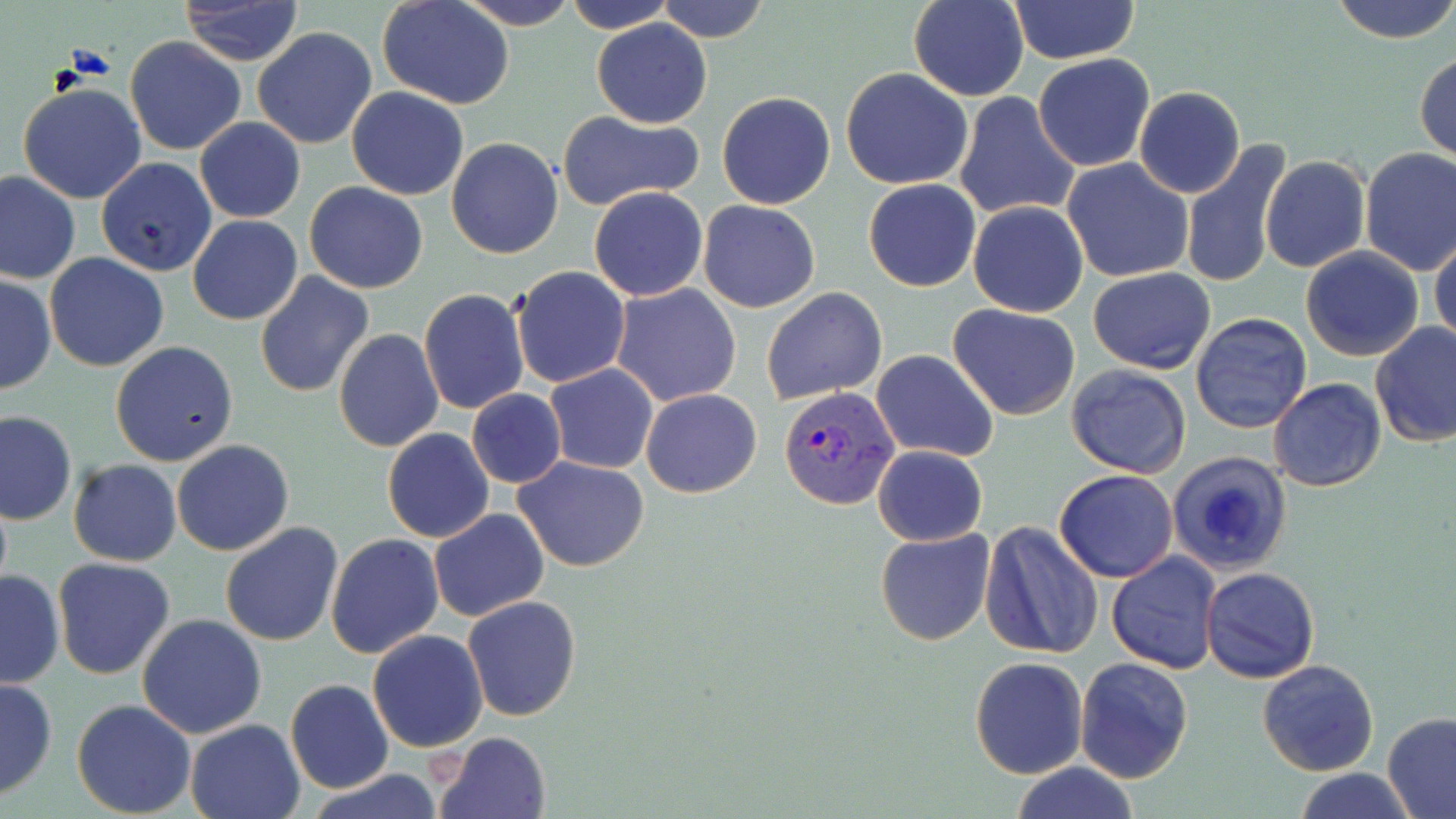

Summary:
  - Coordinate format: approximate bounding boxes as named x1/y1/x2/y2 corners in pixels
  - Uninfected red blood cell locations: (x1=455, y1=0, x2=581, y2=30), (x1=563, y1=0, x2=678, y2=32), (x1=654, y1=0, x2=769, y2=43), (x1=908, y1=0, x2=1030, y2=101), (x1=1008, y1=0, x2=1140, y2=63), (x1=1328, y1=0, x2=1456, y2=45), (x1=378, y1=1, x2=514, y2=109), (x1=179, y1=2, x2=305, y2=65), (x1=591, y1=18, x2=712, y2=128), (x1=252, y1=27, x2=379, y2=149), (x1=125, y1=37, x2=247, y2=157), (x1=1415, y1=50, x2=1456, y2=163), (x1=1033, y1=53, x2=1156, y2=172), (x1=840, y1=68, x2=974, y2=190), (x1=17, y1=81, x2=148, y2=204), (x1=720, y1=81, x2=971, y2=198), (x1=347, y1=86, x2=469, y2=200), (x1=1134, y1=86, x2=1244, y2=199), (x1=716, y1=92, x2=836, y2=209), (x1=955, y1=93, x2=1079, y2=219), (x1=1159, y1=109, x2=1275, y2=248), (x1=557, y1=110, x2=703, y2=213), (x1=194, y1=118, x2=306, y2=222), (x1=446, y1=138, x2=563, y2=258), (x1=1180, y1=142, x2=1292, y2=289), (x1=1358, y1=148, x2=1456, y2=276), (x1=1260, y1=156, x2=1370, y2=273), (x1=96, y1=157, x2=217, y2=276), (x1=1062, y1=157, x2=1195, y2=283), (x1=1, y1=171, x2=81, y2=286), (x1=862, y1=177, x2=981, y2=292), (x1=304, y1=182, x2=430, y2=293), (x1=589, y1=186, x2=709, y2=300), (x1=697, y1=200, x2=820, y2=314), (x1=967, y1=201, x2=1089, y2=317), (x1=188, y1=215, x2=303, y2=325), (x1=1430, y1=232, x2=1455, y2=353), (x1=211, y1=241, x2=355, y2=378), (x1=1300, y1=248, x2=1424, y2=361), (x1=43, y1=254, x2=169, y2=372), (x1=512, y1=265, x2=630, y2=388), (x1=1088, y1=267, x2=1216, y2=375), (x1=254, y1=273, x2=374, y2=397), (x1=0, y1=274, x2=57, y2=395), (x1=611, y1=283, x2=743, y2=407), (x1=761, y1=287, x2=888, y2=404), (x1=418, y1=288, x2=529, y2=415), (x1=948, y1=303, x2=1081, y2=420), (x1=1189, y1=313, x2=1312, y2=433), (x1=1369, y1=322, x2=1456, y2=447), (x1=334, y1=328, x2=444, y2=450), (x1=110, y1=341, x2=239, y2=466), (x1=871, y1=349, x2=999, y2=461), (x1=1065, y1=364, x2=1193, y2=478), (x1=544, y1=365, x2=659, y2=474), (x1=1269, y1=377, x2=1386, y2=492), (x1=641, y1=387, x2=763, y2=497), (x1=466, y1=390, x2=566, y2=487), (x1=0, y1=409, x2=77, y2=524), (x1=383, y1=429, x2=494, y2=543), (x1=171, y1=439, x2=295, y2=556), (x1=872, y1=445, x2=989, y2=546), (x1=1167, y1=449, x2=1294, y2=578), (x1=512, y1=455, x2=652, y2=572), (x1=67, y1=459, x2=181, y2=567), (x1=1054, y1=469, x2=1179, y2=582), (x1=429, y1=507, x2=549, y2=621), (x1=980, y1=520, x2=1103, y2=660), (x1=220, y1=521, x2=344, y2=647), (x1=875, y1=525, x2=996, y2=646), (x1=326, y1=533, x2=444, y2=658), (x1=436, y1=533, x2=570, y2=691), (x1=1106, y1=551, x2=1222, y2=674), (x1=52, y1=557, x2=177, y2=680), (x1=1199, y1=566, x2=1321, y2=684), (x1=0, y1=568, x2=64, y2=689), (x1=462, y1=596, x2=581, y2=721), (x1=137, y1=613, x2=268, y2=739), (x1=368, y1=629, x2=488, y2=752), (x1=970, y1=656, x2=1088, y2=777), (x1=1076, y1=657, x2=1194, y2=785), (x1=1258, y1=658, x2=1380, y2=776), (x1=0, y1=676, x2=58, y2=801), (x1=284, y1=679, x2=394, y2=796), (x1=71, y1=699, x2=197, y2=818), (x1=1382, y1=712, x2=1456, y2=818), (x1=185, y1=718, x2=306, y2=819), (x1=434, y1=730, x2=552, y2=818), (x1=1010, y1=762, x2=1138, y2=819), (x1=1291, y1=768, x2=1417, y2=819), (x1=309, y1=770, x2=446, y2=819)
  - Plasmodium vivax-infected red blood cell locations: (x1=776, y1=386, x2=901, y2=510)
  - Slide-level diagnosis: Plasmodium vivax
  - Preparation: thin blood film
  - Stain: May-Grünwald-Giemsa
  - Magnification: 1000x
  - Image size: 1456×819 pixels
  - Modality: light microscopy
  - Field of view: one of a larger specimen